State the blood parasite species.
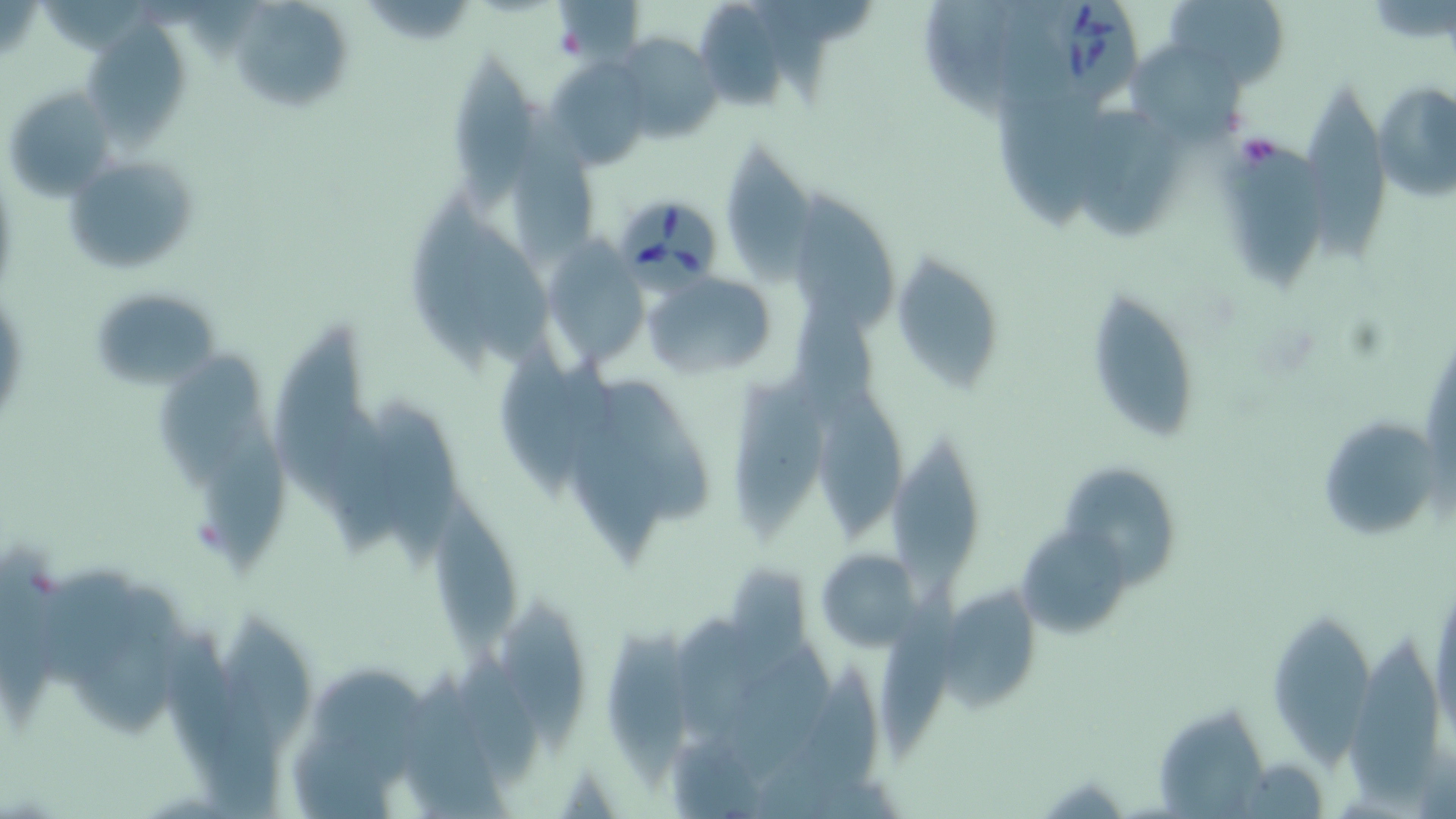
Babesia divergens.

stain = May-Grünwald-Giemsa
platelet locations = approximate bounding boxes as (x1, y1, x2, y2) in pixels: (550, 20, 591, 62), (1234, 131, 1284, 174)
magnification = 1000x
field of view = one of a larger specimen
Babesia divergens-infected red blood cell locations = approximate bounding boxes as (x1, y1, x2, y2) in pixels: (1039, 0, 1143, 109), (617, 196, 721, 305)
modality = optical microscopy
image size = 1456×819 pixels
uninfected red blood cell locations = approximate bounding boxes as (x1, y1, x2, y2) in pixels: (1164, 0, 1289, 89), (695, 3, 789, 111), (235, 5, 350, 112), (89, 16, 186, 156), (614, 34, 722, 144), (452, 49, 534, 211), (1136, 50, 1248, 147), (546, 58, 650, 166), (1373, 82, 1456, 202), (1307, 83, 1394, 262), (2, 84, 116, 202), (996, 92, 1111, 234), (514, 108, 606, 262), (1075, 112, 1185, 239), (725, 137, 816, 295), (1217, 145, 1333, 298), (69, 158, 197, 275), (787, 191, 898, 342), (407, 193, 493, 371), (466, 226, 564, 380), (541, 241, 649, 372), (889, 249, 1006, 392), (641, 269, 780, 380), (88, 287, 221, 391), (1086, 287, 1203, 443), (275, 320, 363, 502), (159, 351, 260, 489), (499, 351, 587, 497), (728, 375, 830, 546), (595, 379, 715, 530), (816, 388, 909, 542), (379, 399, 461, 573), (200, 407, 291, 579), (325, 407, 415, 557), (1315, 413, 1444, 542), (885, 429, 983, 601), (1063, 463, 1180, 587), (433, 490, 518, 662), (1020, 525, 1129, 636), (0, 536, 67, 723), (815, 548, 920, 649), (40, 569, 147, 692), (83, 581, 186, 733), (877, 581, 955, 766), (1430, 582, 1456, 747), (939, 586, 1041, 712), (502, 602, 593, 753), (210, 610, 320, 761), (667, 614, 777, 740), (1271, 616, 1374, 771), (606, 623, 702, 786), (1349, 625, 1439, 800), (729, 645, 831, 787), (457, 653, 544, 787), (756, 662, 884, 816), (395, 666, 509, 815), (316, 667, 433, 789), (1156, 705, 1263, 819), (288, 721, 402, 819)
preparation = thin blood smear